Classify this cell by malaria status.
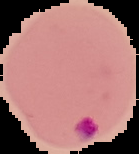

It is parasitized.

preparation: thin blood film
image_size: 139×154 pixels
image_type: cell region segmented out of the field of view; surrounding area masked to black